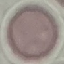
malaria_status: uninfected
preparation: thin blood smear
stain: Giemsa
capture: smartphone through the microscope eyepiece
image_type: cell patch, automatically extracted from a larger field of view and resized to 64 × 64 pixels